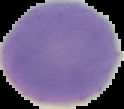

Summary:
  - Image size: 124×109 pixels
  - Image type: segmented cell region with the area outside set to black
  - Malaria status: uninfected
  - Preparation: thin blood film